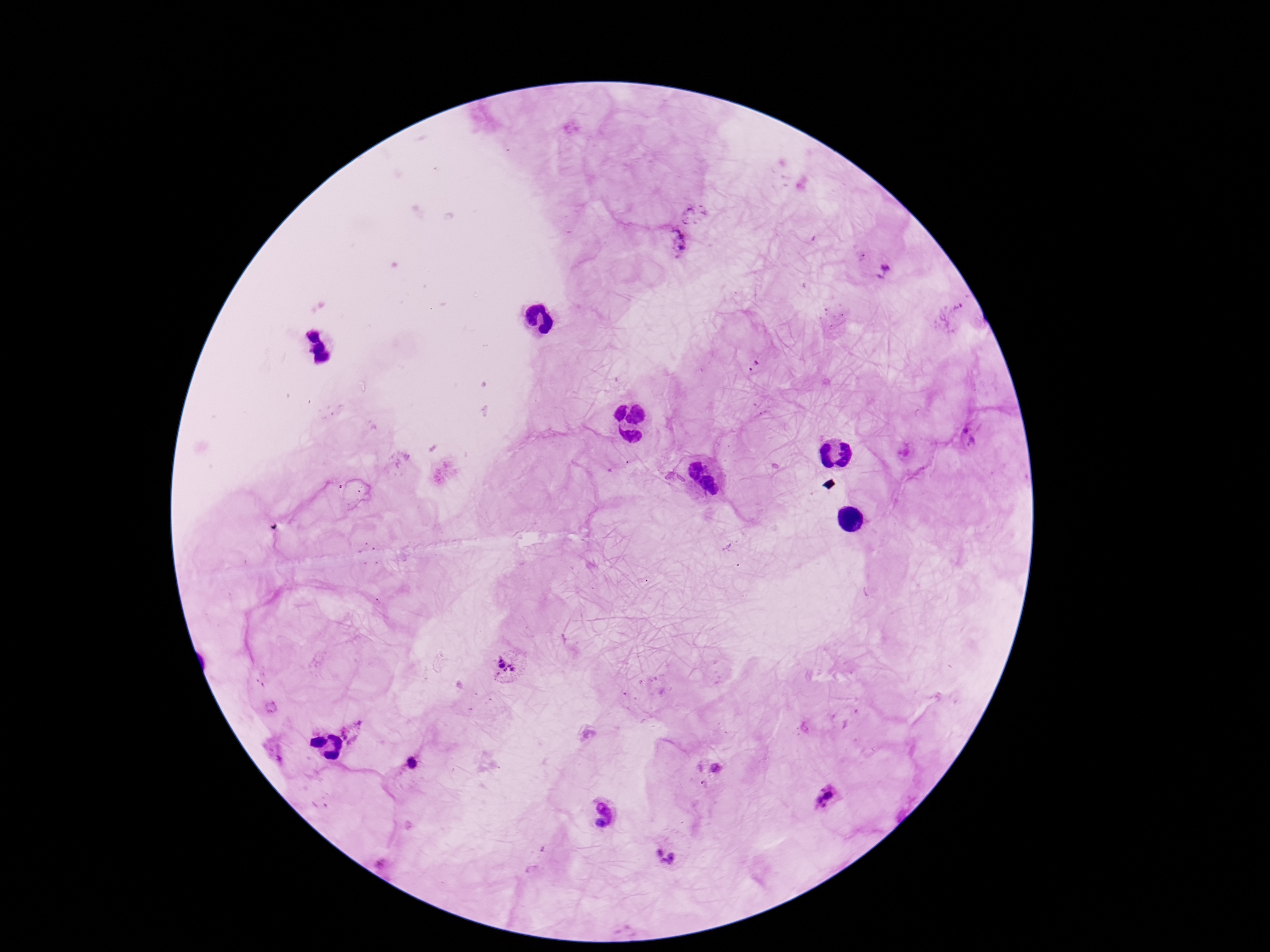

Approximate centers as [x, y] in pixels. Plasmodium parasite locations: [696, 212], [677, 242], [884, 272], [753, 366], [968, 435], [506, 668], [355, 732], [412, 765], [716, 768], [827, 798], [667, 855]. 100x magnification. Patient malaria status: positive. Giemsa stain. One field from this slide. Thick blood film. Image is 1270×952 pixels. Photographed through the microscope eyepiece with a smartphone camera.